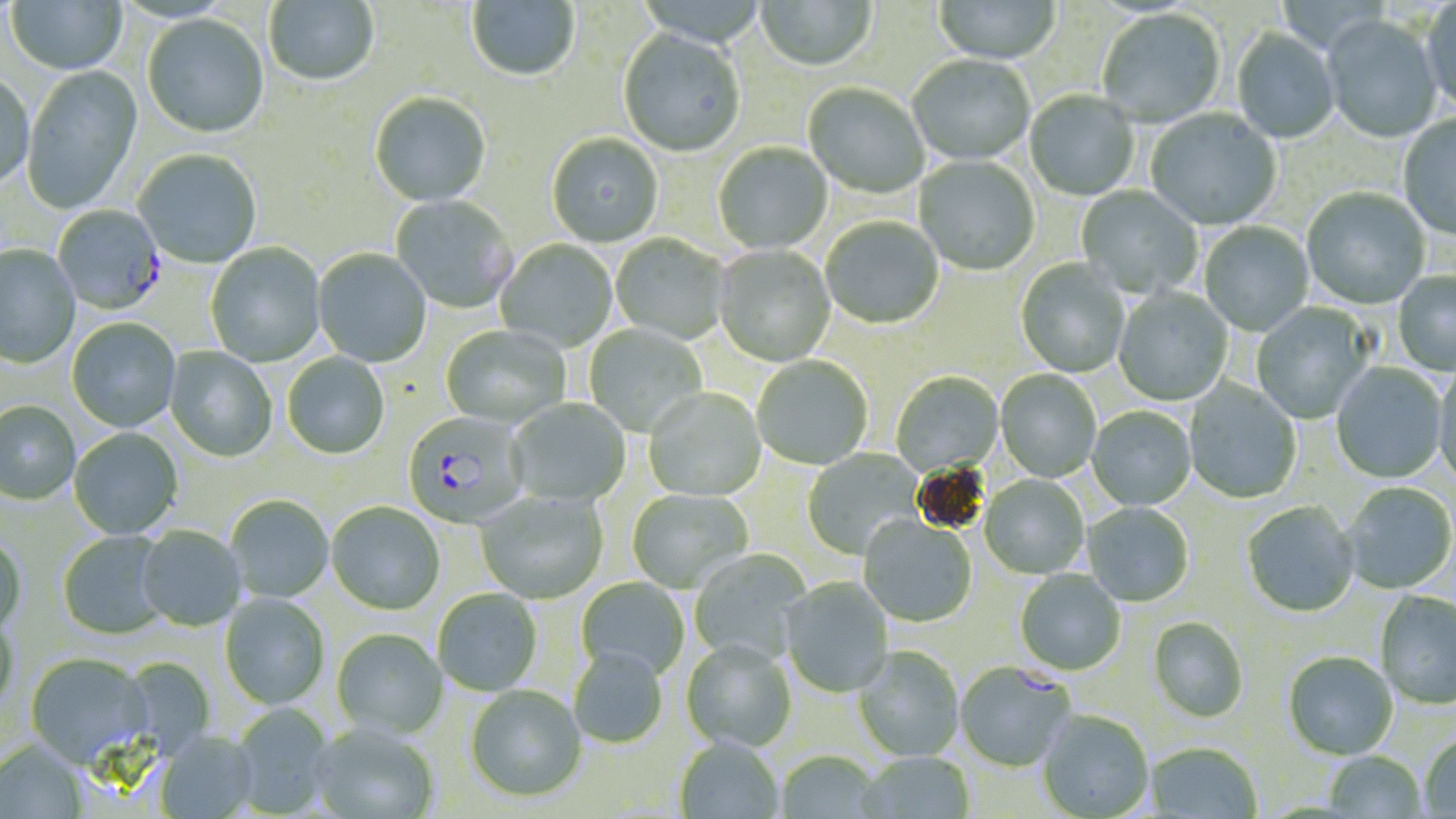 Approximate bounding boxes as named x1/y1/x2/y2 corners in pixels. Plasmodium falciparum-infected red blood cell locations: (x1=52, y1=204, x2=166, y2=316), (x1=402, y1=413, x2=529, y2=529), (x1=956, y1=662, x2=1075, y2=772). Uninfected red blood cell locations: (x1=7, y1=0, x2=127, y2=76), (x1=265, y1=0, x2=379, y2=88), (x1=755, y1=0, x2=876, y2=73), (x1=1421, y1=0, x2=1456, y2=115), (x1=467, y1=1, x2=580, y2=83), (x1=933, y1=1, x2=1060, y2=66), (x1=1097, y1=10, x2=1226, y2=129), (x1=142, y1=15, x2=270, y2=140), (x1=1322, y1=16, x2=1443, y2=145), (x1=1232, y1=29, x2=1339, y2=144), (x1=618, y1=31, x2=746, y2=158), (x1=908, y1=56, x2=1034, y2=166), (x1=22, y1=65, x2=144, y2=216), (x1=0, y1=74, x2=34, y2=193), (x1=803, y1=83, x2=929, y2=199), (x1=1025, y1=92, x2=1139, y2=201), (x1=370, y1=93, x2=492, y2=207), (x1=1145, y1=108, x2=1282, y2=230), (x1=1398, y1=115, x2=1456, y2=242), (x1=547, y1=134, x2=663, y2=248), (x1=713, y1=143, x2=832, y2=255), (x1=133, y1=150, x2=262, y2=269), (x1=914, y1=156, x2=1040, y2=276), (x1=1076, y1=185, x2=1202, y2=299), (x1=1302, y1=188, x2=1430, y2=310), (x1=390, y1=195, x2=517, y2=314), (x1=820, y1=218, x2=944, y2=330), (x1=1199, y1=221, x2=1314, y2=336), (x1=611, y1=234, x2=730, y2=344), (x1=495, y1=240, x2=617, y2=352), (x1=206, y1=243, x2=326, y2=367), (x1=0, y1=245, x2=81, y2=369), (x1=714, y1=245, x2=836, y2=367), (x1=312, y1=249, x2=432, y2=368), (x1=1015, y1=258, x2=1129, y2=378), (x1=1392, y1=272, x2=1456, y2=376), (x1=1113, y1=288, x2=1232, y2=406), (x1=1250, y1=302, x2=1375, y2=424), (x1=67, y1=319, x2=181, y2=432), (x1=584, y1=325, x2=707, y2=436), (x1=441, y1=326, x2=569, y2=428), (x1=164, y1=346, x2=277, y2=462), (x1=282, y1=353, x2=390, y2=460), (x1=752, y1=356, x2=872, y2=471), (x1=1433, y1=362, x2=1456, y2=490), (x1=1330, y1=363, x2=1447, y2=483), (x1=995, y1=370, x2=1101, y2=482), (x1=891, y1=372, x2=1004, y2=477), (x1=1184, y1=379, x2=1303, y2=504), (x1=644, y1=389, x2=767, y2=501), (x1=507, y1=398, x2=631, y2=507), (x1=0, y1=403, x2=80, y2=507), (x1=1087, y1=406, x2=1196, y2=511), (x1=69, y1=428, x2=183, y2=540), (x1=802, y1=448, x2=923, y2=559), (x1=979, y1=476, x2=1089, y2=579), (x1=1341, y1=483, x2=1456, y2=595), (x1=626, y1=489, x2=754, y2=594), (x1=474, y1=492, x2=609, y2=604), (x1=226, y1=495, x2=334, y2=602), (x1=1242, y1=502, x2=1359, y2=618), (x1=326, y1=503, x2=446, y2=616), (x1=1083, y1=503, x2=1194, y2=608), (x1=858, y1=518, x2=977, y2=627), (x1=136, y1=527, x2=246, y2=632), (x1=57, y1=532, x2=172, y2=641), (x1=0, y1=537, x2=28, y2=638), (x1=689, y1=549, x2=811, y2=666), (x1=1014, y1=570, x2=1126, y2=677), (x1=576, y1=577, x2=689, y2=682), (x1=781, y1=578, x2=894, y2=697), (x1=433, y1=589, x2=543, y2=696), (x1=1375, y1=591, x2=1456, y2=710), (x1=219, y1=594, x2=329, y2=710), (x1=0, y1=614, x2=19, y2=715), (x1=1148, y1=617, x2=1248, y2=723), (x1=331, y1=630, x2=448, y2=740), (x1=681, y1=642, x2=797, y2=753), (x1=853, y1=647, x2=965, y2=762), (x1=569, y1=651, x2=668, y2=749), (x1=1284, y1=652, x2=1398, y2=760), (x1=25, y1=654, x2=153, y2=770), (x1=118, y1=656, x2=215, y2=759), (x1=465, y1=686, x2=587, y2=804), (x1=231, y1=703, x2=335, y2=816), (x1=1037, y1=711, x2=1155, y2=819), (x1=311, y1=724, x2=439, y2=819), (x1=155, y1=733, x2=260, y2=819), (x1=1419, y1=734, x2=1456, y2=817), (x1=674, y1=738, x2=784, y2=819), (x1=0, y1=742, x2=87, y2=819), (x1=1145, y1=742, x2=1262, y2=819), (x1=1323, y1=750, x2=1427, y2=818), (x1=776, y1=751, x2=885, y2=818), (x1=854, y1=752, x2=975, y2=819). Slide-level diagnosis: Plasmodium falciparum. Image is 1456×819 pixels. Optical microscopy. Thin blood film. May-Grünwald-Giemsa-stained preparation. 1000x magnification. One field of a larger specimen.